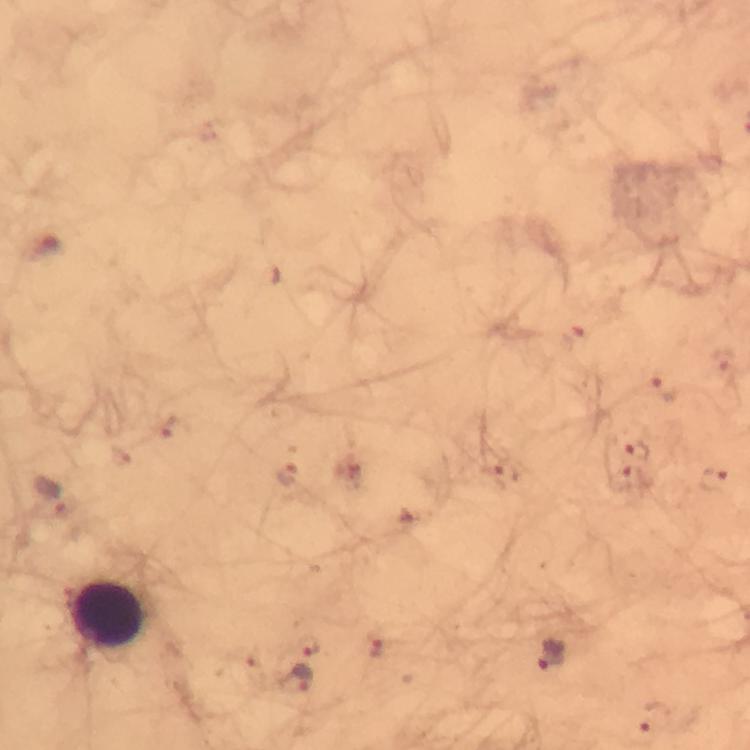

Approximate centers as [x, y] in pixels.
Summary:
  - Malaria parasite locations: [571, 336], [724, 363], [665, 388], [637, 449], [288, 473], [503, 475], [625, 476], [712, 477], [51, 497], [308, 645], [550, 655], [295, 678], [653, 717]
  - Leukocyte locations: [104, 613]
  - Context: from a diagnostic examination for malaria
  - Immersion oil: used
  - Image size: 750×750 pixels
  - Magnification: 100x
  - Cropped from: a single field of view
  - Preparation: thick blood film
  - Capture: smartphone camera through the microscope
  - Stain: Giemsa